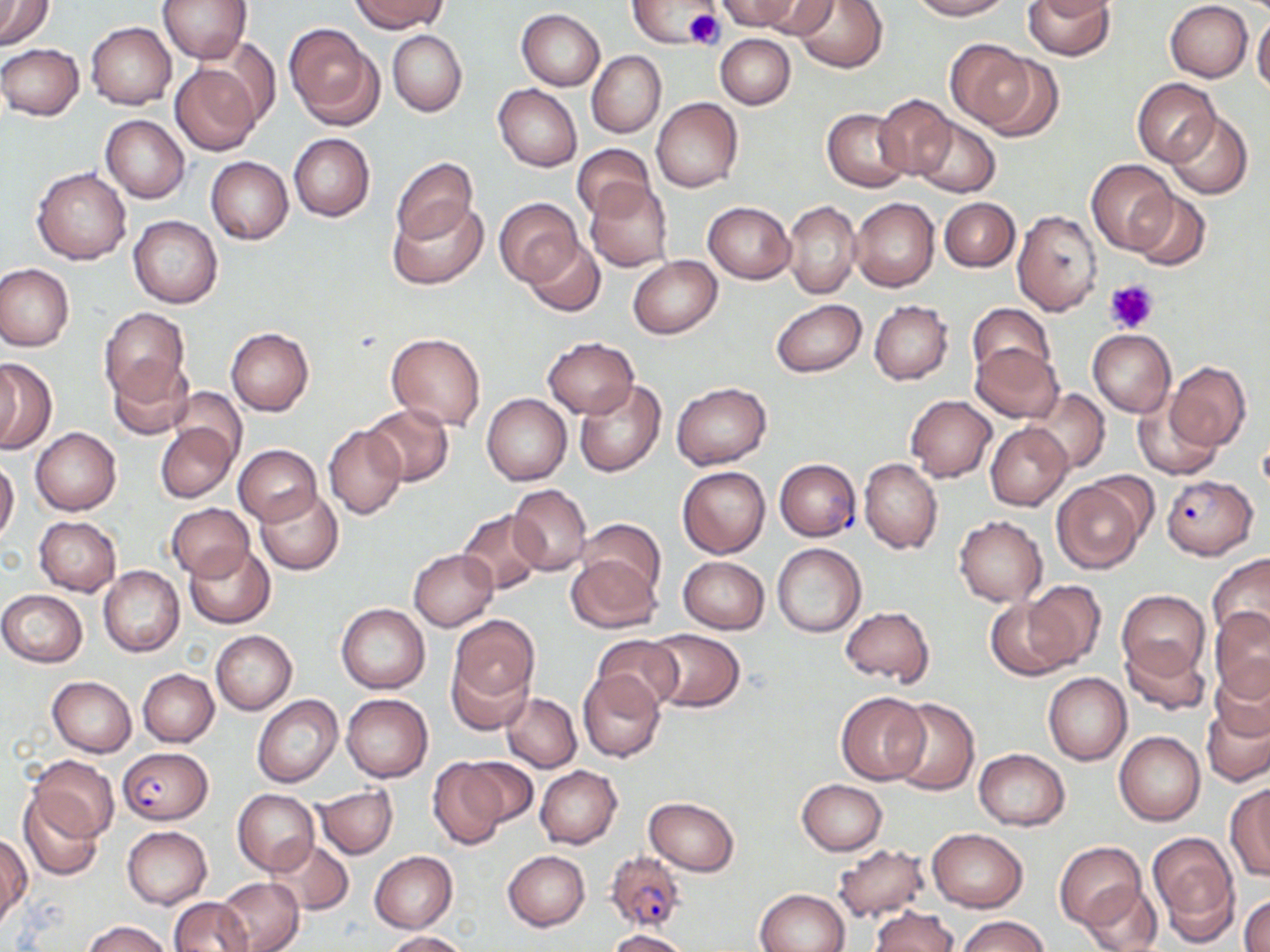
slide_level_diagnosis: Plasmodium falciparum
modality: light microscopy
stain: May-Grünwald-Giemsa
preparation: thin blood smear
uninfected_red_blood_cell_locations: 'approximate bounding boxes as [x1, y1, x2, y2] in pixels: [0, 0, 54, 49], [157, 0, 252, 63], [351, 0, 447, 33], [628, 0, 714, 49], [716, 0, 800, 32], [756, 0, 838, 38], [793, 0, 887, 72], [909, 0, 1009, 20], [1022, 0, 1114, 59], [1165, 2, 1252, 82], [512, 8, 595, 170], [517, 9, 605, 90], [1252, 14, 1270, 96], [86, 22, 175, 110], [286, 25, 381, 129], [387, 31, 466, 116], [715, 33, 796, 109], [946, 37, 1042, 132], [1, 43, 84, 120], [587, 51, 666, 137], [976, 54, 1063, 141], [170, 63, 262, 155], [1133, 78, 1221, 167], [494, 84, 581, 172], [875, 94, 957, 178], [652, 98, 743, 192], [823, 108, 912, 191], [1166, 111, 1254, 200], [101, 115, 189, 202], [911, 117, 1000, 198], [289, 133, 375, 221], [572, 143, 655, 222], [205, 156, 293, 244], [392, 157, 476, 243], [1087, 160, 1178, 256], [33, 168, 131, 265], [585, 181, 675, 272], [1131, 190, 1211, 270], [850, 197, 939, 291], [389, 198, 488, 289], [940, 198, 1019, 272], [495, 199, 583, 287], [783, 201, 861, 299], [704, 202, 795, 283], [1012, 210, 1102, 316], [129, 215, 223, 308], [523, 239, 606, 317], [628, 256, 721, 338], [0, 265, 74, 351], [771, 298, 866, 378], [868, 300, 953, 384], [966, 303, 1056, 383], [100, 307, 189, 399], [226, 328, 314, 415], [1088, 329, 1176, 417], [387, 332, 486, 430], [543, 337, 639, 418], [970, 344, 1064, 422], [106, 357, 194, 439], [0, 358, 56, 454], [1166, 362, 1251, 450], [574, 380, 666, 479], [671, 382, 771, 468], [1027, 388, 1110, 473], [169, 389, 247, 468], [483, 393, 571, 486], [906, 396, 997, 481], [1131, 399, 1221, 481], [360, 403, 455, 486], [156, 422, 237, 503], [986, 422, 1072, 510], [325, 425, 407, 519], [30, 427, 120, 515], [234, 444, 322, 525], [0, 458, 19, 545], [858, 459, 942, 553], [678, 466, 770, 559], [1052, 479, 1146, 573], [506, 484, 593, 575], [255, 487, 342, 576], [166, 504, 253, 581], [458, 509, 546, 595], [34, 516, 122, 595], [954, 516, 1047, 606], [577, 519, 666, 599], [184, 543, 276, 628], [772, 543, 867, 637], [409, 549, 498, 629], [1208, 554, 1270, 644], [567, 556, 661, 633], [677, 556, 771, 634], [98, 565, 185, 657], [1021, 580, 1107, 673], [1, 590, 86, 666], [1117, 590, 1210, 679], [985, 597, 1071, 681], [337, 603, 430, 693], [840, 606, 934, 685], [1209, 608, 1270, 702], [448, 615, 539, 711], [211, 629, 297, 715], [644, 630, 745, 711], [591, 634, 682, 711], [1118, 637, 1210, 717], [447, 653, 531, 735], [137, 669, 219, 746], [578, 672, 666, 761], [1043, 673, 1131, 764], [47, 677, 136, 757], [1201, 690, 1270, 789], [836, 691, 931, 785], [341, 692, 433, 782], [502, 693, 582, 772], [253, 694, 342, 788], [889, 697, 979, 795], [1115, 730, 1205, 826], [974, 748, 1070, 830], [29, 756, 117, 842], [463, 756, 538, 828], [427, 758, 509, 850], [535, 765, 622, 849], [795, 779, 888, 855], [1225, 784, 1270, 881], [314, 785, 397, 858], [232, 789, 319, 874], [18, 790, 105, 880], [644, 797, 740, 875], [122, 825, 212, 909], [927, 828, 1028, 911], [1147, 832, 1240, 943], [1, 833, 31, 926], [268, 838, 354, 914], [1054, 842, 1146, 930], [833, 843, 929, 922], [370, 851, 458, 933], [502, 851, 590, 932], [216, 876, 304, 952], [1080, 882, 1164, 952], [755, 888, 851, 952], [1241, 895, 1269, 952], [168, 897, 253, 951], [870, 906, 958, 952], [957, 915, 1048, 952], [84, 921, 169, 952], [606, 929, 692, 952], [383, 930, 469, 951]'
image_size: 1270×952 pixels
platelet_locations: 'approximate bounding boxes as [x1, y1, x2, y2] in pixels: [684, 9, 725, 50], [1105, 279, 1158, 334]'
field_of_view: single
plasmodium_falciparum_infected_red_blood_cell_locations: 'approximate bounding boxes as [x1, y1, x2, y2] in pixels: [773, 458, 862, 541], [1160, 474, 1258, 560], [117, 747, 213, 824], [605, 851, 683, 931]'
magnification: 1000x